Classify this cell by malaria status.
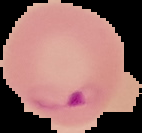
Parasitized.

image_type: segmented cell region with the area outside set to black
preparation: thin blood smear
image_size: 142×133 pixels